Report the malaria status of this cell.
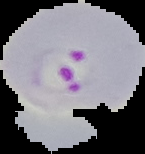
It is parasitized.

image type = cell region segmented out of the field of view; surrounding area masked to black
image size = 145×154 pixels
preparation = thin blood film